Classify this cell by malaria status.
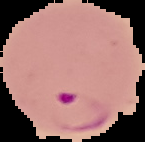
It is parasitized.

From a thin blood film. The area outside the segmented cell region is set to black. Image is 145×142 pixels.